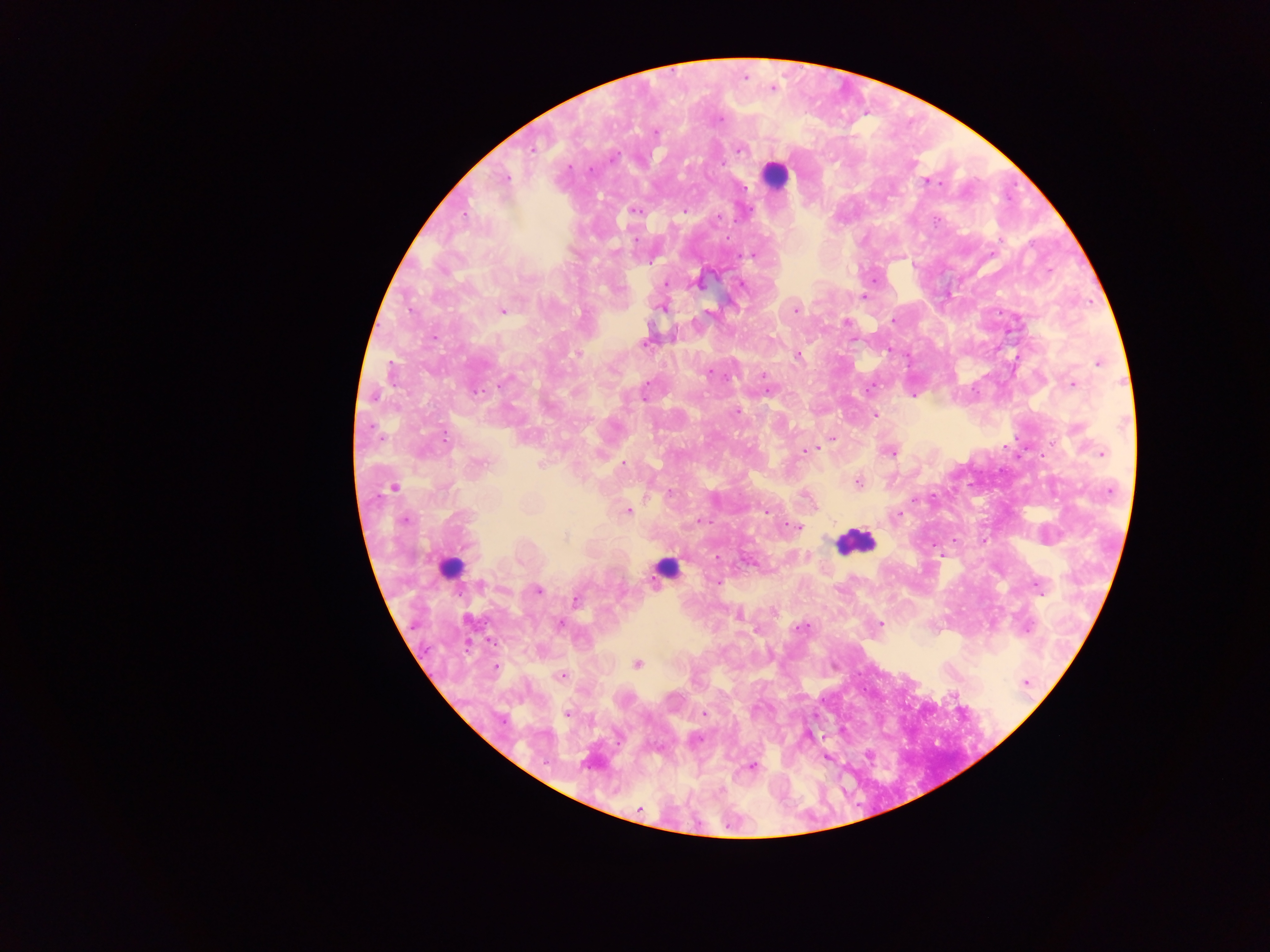

Approximate centers as {x, y} in pixels. Leukocyte locations: {774, 174}, {854, 541}, {449, 567}, {665, 567}. Plasmodium parasite locations: {655, 131}, {532, 148}, {739, 150}, {589, 170}, {504, 179}, {926, 181}, {684, 210}, {634, 211}, {938, 220}, {751, 254}, {876, 280}, {700, 281}, {666, 283}, {740, 283}, {862, 296}, {663, 307}, {796, 310}, {501, 311}, {893, 321}, {844, 322}, {645, 341}, {577, 354}, {797, 354}, {1098, 362}, {709, 373}, {763, 375}, {1073, 384}, {871, 387}, {767, 391}, {913, 395}, {644, 397}, {736, 410}, {875, 414}, {832, 439}, {807, 451}, {890, 451}, {1102, 453}, {478, 464}, {623, 465}, {858, 481}, {394, 487}, {764, 509}, {628, 510}, {897, 514}, {403, 520}, {699, 521}, {796, 527}, {566, 536}, {939, 554}, {718, 558}, {717, 581}, {1038, 586}, {537, 590}, {577, 599}, {738, 613}, {880, 623}, {558, 624}, {801, 627}, {637, 663}, {559, 676}, {1026, 682}, {703, 713}, {567, 714}, {809, 735}, {696, 739}, {826, 756}, {751, 765}, {639, 808}. Single field of view. Collected in Ghana. Thick blood film. Image is 1270×952 pixels. Photographed through a microscope with a mobile-phone camera.